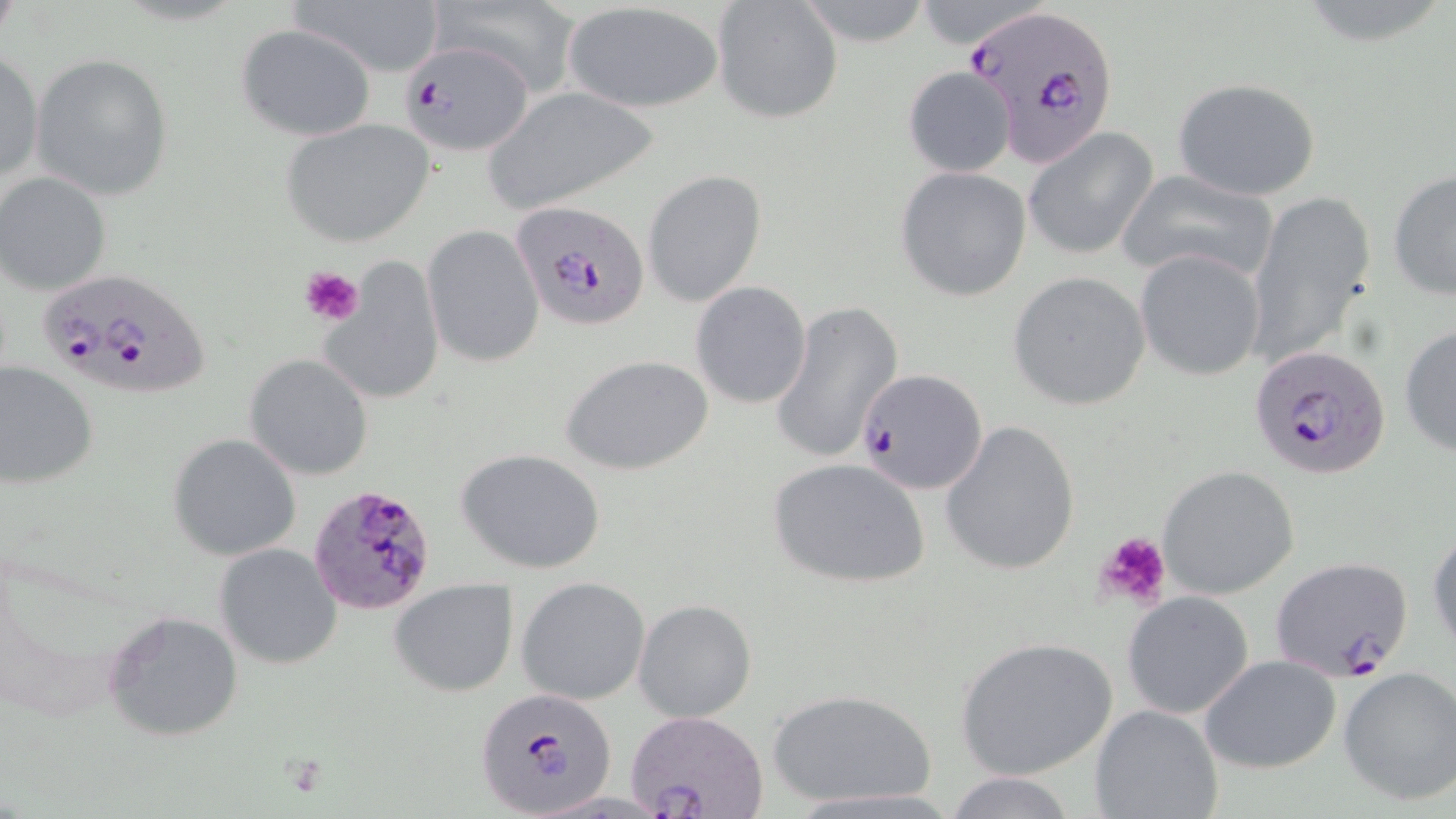

Summary:
  - Coordinate format: approximate bounding boxes as named x1/y1/x2/y2 corners in pixels
  - Plasmodium falciparum-infected red blood cell locations: (x1=965, y1=3, x2=1121, y2=165), (x1=399, y1=41, x2=531, y2=158), (x1=510, y1=199, x2=645, y2=331), (x1=35, y1=267, x2=213, y2=399), (x1=1250, y1=344, x2=1391, y2=481), (x1=857, y1=368, x2=986, y2=495), (x1=308, y1=484, x2=439, y2=616), (x1=1271, y1=555, x2=1415, y2=683), (x1=474, y1=686, x2=619, y2=817), (x1=624, y1=710, x2=770, y2=819)
  - Uninfected red blood cell locations: (x1=288, y1=0, x2=447, y2=78), (x1=435, y1=0, x2=582, y2=95), (x1=794, y1=0, x2=935, y2=48), (x1=711, y1=1, x2=842, y2=125), (x1=562, y1=3, x2=725, y2=114), (x1=235, y1=23, x2=376, y2=140), (x1=0, y1=52, x2=43, y2=188), (x1=30, y1=54, x2=174, y2=200), (x1=902, y1=66, x2=1017, y2=177), (x1=1173, y1=77, x2=1321, y2=200), (x1=481, y1=87, x2=659, y2=211), (x1=280, y1=118, x2=436, y2=249), (x1=1023, y1=129, x2=1157, y2=262), (x1=895, y1=166, x2=1032, y2=302), (x1=1114, y1=166, x2=1279, y2=286), (x1=1387, y1=167, x2=1456, y2=304), (x1=643, y1=169, x2=768, y2=307), (x1=1, y1=171, x2=116, y2=296), (x1=1244, y1=189, x2=1377, y2=370), (x1=422, y1=224, x2=544, y2=368), (x1=1135, y1=249, x2=1265, y2=381), (x1=325, y1=252, x2=444, y2=406), (x1=1008, y1=270, x2=1151, y2=411), (x1=691, y1=281, x2=812, y2=408), (x1=771, y1=299, x2=903, y2=467), (x1=1399, y1=322, x2=1456, y2=456), (x1=245, y1=352, x2=375, y2=480), (x1=560, y1=354, x2=713, y2=476), (x1=0, y1=361, x2=98, y2=490), (x1=940, y1=418, x2=1082, y2=577), (x1=168, y1=433, x2=302, y2=561), (x1=459, y1=450, x2=606, y2=574), (x1=768, y1=457, x2=931, y2=589), (x1=1157, y1=465, x2=1300, y2=598), (x1=1427, y1=526, x2=1456, y2=656), (x1=213, y1=543, x2=344, y2=669), (x1=516, y1=576, x2=651, y2=705), (x1=390, y1=579, x2=516, y2=697), (x1=1121, y1=592, x2=1254, y2=720), (x1=633, y1=599, x2=757, y2=723), (x1=103, y1=608, x2=243, y2=742), (x1=953, y1=636, x2=1118, y2=782), (x1=1199, y1=654, x2=1342, y2=775), (x1=1338, y1=667, x2=1456, y2=806), (x1=769, y1=687, x2=937, y2=809), (x1=1090, y1=704, x2=1224, y2=819), (x1=942, y1=773, x2=1079, y2=819)
  - Platelet locations: (x1=301, y1=265, x2=363, y2=327), (x1=1091, y1=530, x2=1173, y2=614)
  - Slide-level diagnosis: Plasmodium falciparum
  - Image size: 1456×819 pixels
  - Modality: light microscopy
  - Stain: May-Grünwald-Giemsa
  - Field of view: single
  - Preparation: thin blood film
  - Magnification: 1000x